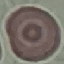
result = no malaria parasites seen
capture = smartphone through the microscope eyepiece
image type = automatically extracted cell patch, resized to 64 × 64 pixels
stain = Giemsa
preparation = thin smear